Give the extent of all uninfected red blood cells.
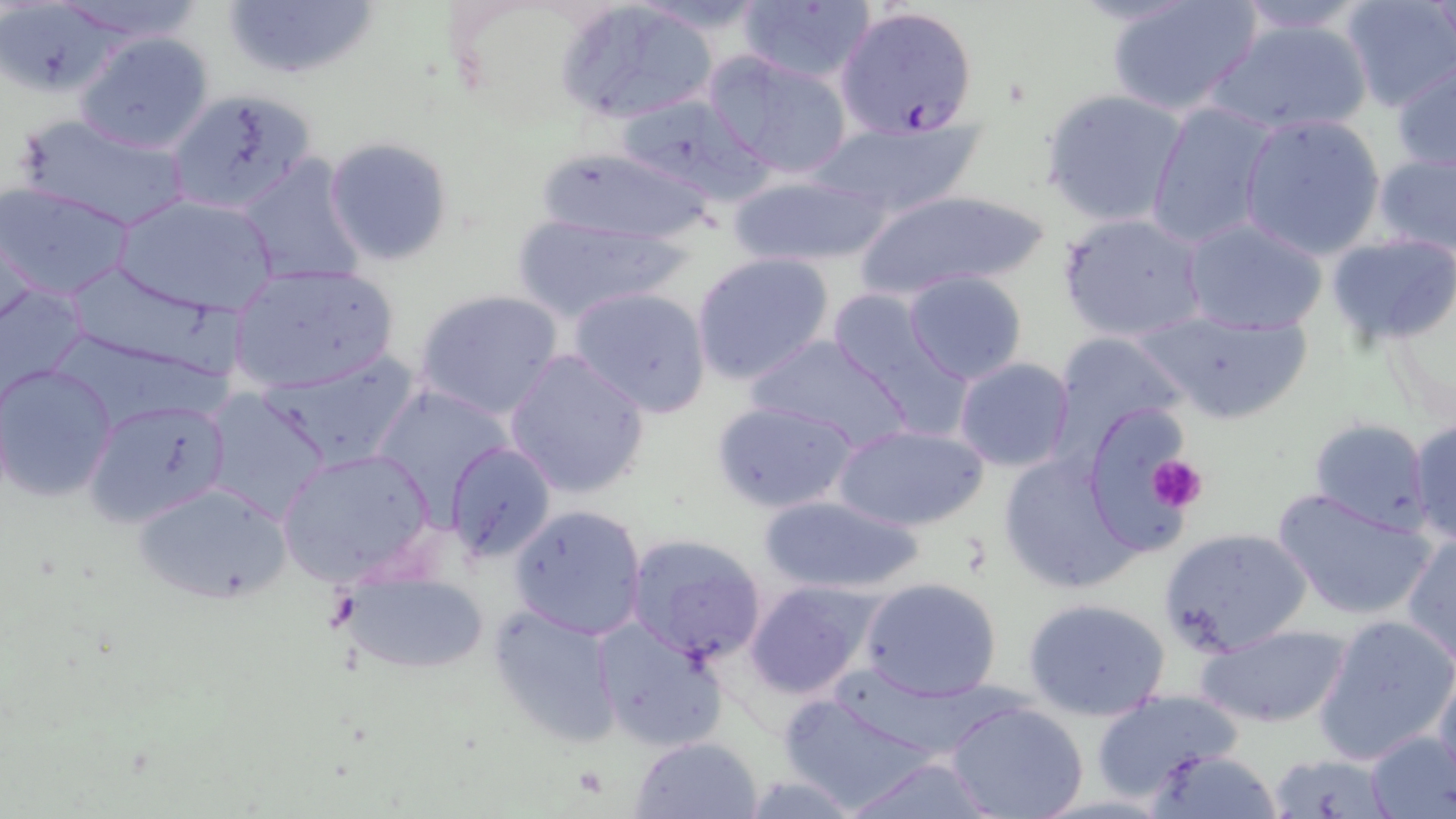

Approximate bounding boxes as (x1, y1, x2, y2) in pixels.
Uninfected red blood cells: (735, 0, 878, 85), (1103, 0, 1265, 118), (1226, 0, 1381, 36), (1339, 0, 1456, 114), (223, 1, 377, 83), (556, 3, 722, 125), (1207, 16, 1377, 138), (75, 32, 215, 154), (706, 53, 853, 180), (1392, 59, 1456, 173), (1040, 88, 1190, 229), (168, 90, 315, 213), (616, 92, 773, 207), (1145, 98, 1277, 249), (1238, 112, 1390, 258), (12, 114, 196, 234), (811, 116, 990, 219), (324, 137, 455, 267), (535, 145, 721, 246), (1372, 150, 1456, 260), (234, 154, 367, 285), (725, 171, 893, 268), (0, 182, 136, 301), (851, 186, 1055, 301), (116, 194, 280, 316), (1058, 212, 1211, 344), (511, 214, 678, 323), (1182, 215, 1329, 335), (1326, 231, 1456, 349), (691, 253, 835, 385), (226, 263, 401, 396), (61, 270, 241, 378), (903, 271, 1029, 385), (1, 282, 91, 405), (570, 286, 713, 417), (413, 289, 565, 421), (826, 289, 974, 437), (1136, 305, 1316, 426), (1049, 331, 1187, 453), (744, 335, 917, 448), (254, 349, 424, 475), (505, 349, 651, 499), (952, 357, 1075, 473), (0, 365, 118, 501), (369, 383, 521, 517), (203, 389, 331, 522), (82, 397, 232, 529), (711, 400, 859, 515), (1078, 400, 1200, 551), (1408, 416, 1456, 546), (1309, 417, 1431, 533), (833, 422, 990, 532), (445, 442, 558, 563), (276, 447, 437, 585), (997, 451, 1142, 595), (132, 480, 291, 605), (1271, 488, 1435, 621), (755, 493, 930, 596), (508, 504, 648, 641), (1157, 526, 1312, 659), (624, 532, 769, 667), (1402, 532, 1456, 668), (337, 563, 493, 677), (859, 577, 1003, 701), (743, 580, 881, 700), (1023, 597, 1172, 721), (488, 604, 625, 746), (1312, 612, 1456, 765), (592, 617, 729, 752), (1192, 624, 1352, 729), (1431, 659, 1456, 783), (1088, 688, 1248, 803), (773, 691, 948, 815), (945, 700, 1089, 819), (1363, 730, 1456, 818), (630, 735, 764, 819), (1144, 748, 1284, 818), (1266, 751, 1392, 817), (840, 757, 1002, 817).

slide-level diagnosis = Plasmodium falciparum
field of view = single
image size = 1456×819 pixels
modality = optical microscopy
preparation = thin blood film
stain = May-Grünwald-Giemsa
Plasmodium falciparum-infected red blood cell locations = approximate bounding boxes as (x1, y1, x2, y2) in pixels: (835, 6, 978, 138)
platelet locations = approximate bounding boxes as (x1, y1, x2, y2) in pixels: (1147, 454, 1206, 512)
magnification = 1000x